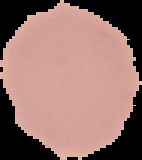
Summary:
  - Preparation: thin blood film
  - Image type: cell region segmented out of the field of view; surrounding area masked to black
  - Result: no Plasmodium parasites detected
  - Image size: 142×160 pixels